Outline each uninfected red blood cell.
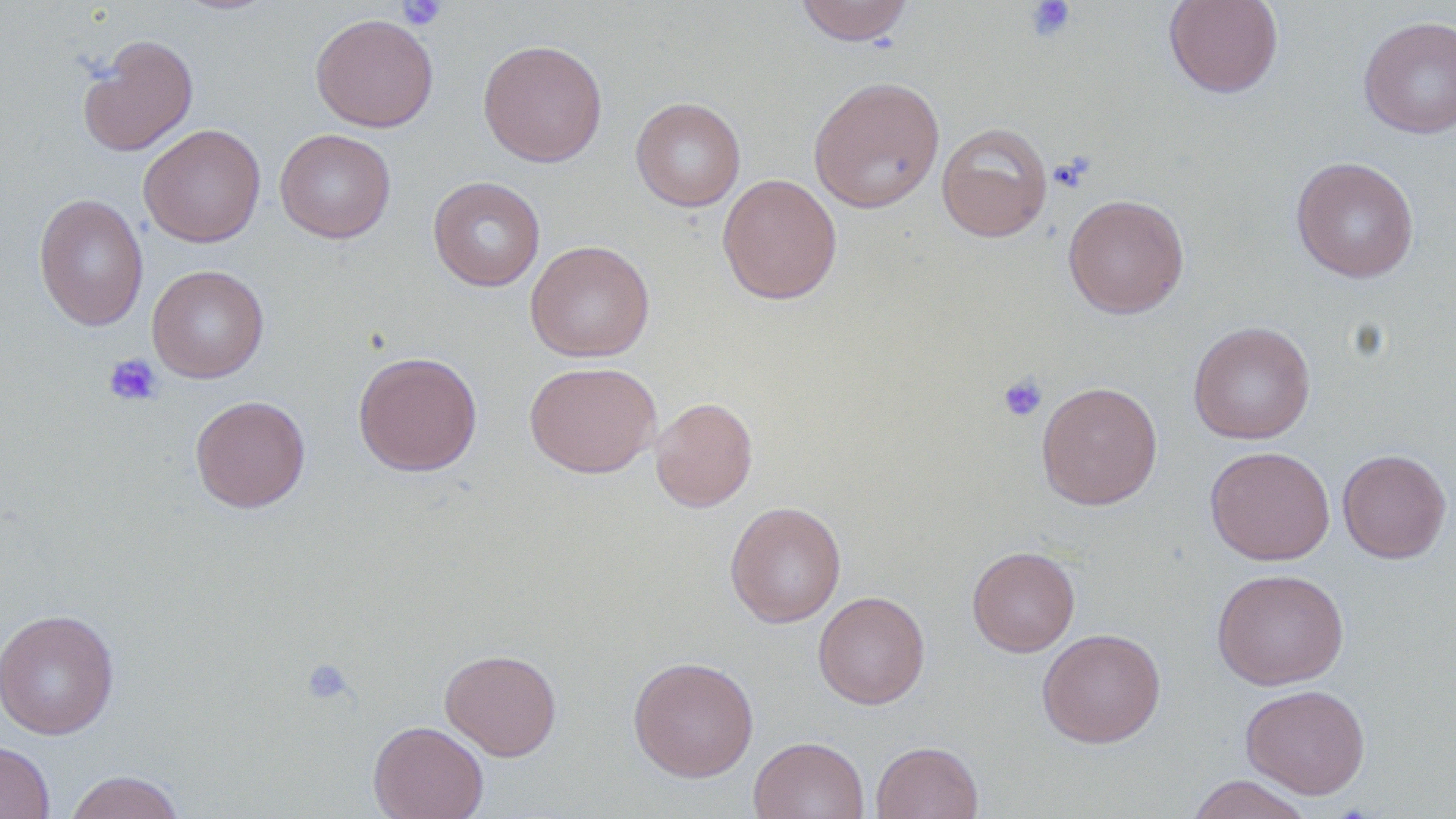
Approximate bounding boxes as (x1, y1, x2, y2) in pixels.
Uninfected red blood cells: (794, 0, 914, 46), (1163, 0, 1284, 98), (310, 13, 439, 132), (1358, 15, 1456, 138), (78, 34, 199, 156), (478, 39, 607, 167), (808, 75, 945, 214), (631, 97, 746, 212), (936, 122, 1053, 242), (138, 123, 266, 247), (275, 128, 396, 244), (1290, 156, 1419, 282), (717, 173, 842, 305), (428, 176, 545, 291), (33, 193, 149, 332), (1062, 193, 1189, 319), (525, 240, 654, 362), (147, 264, 269, 383), (1187, 321, 1316, 444), (353, 351, 483, 476), (523, 360, 661, 478), (1036, 381, 1163, 510), (190, 395, 311, 513), (650, 396, 758, 513), (1205, 446, 1335, 565), (1337, 448, 1452, 563), (725, 501, 847, 628), (967, 545, 1080, 657), (1211, 568, 1349, 690), (813, 591, 929, 709), (0, 608, 120, 740), (1037, 628, 1165, 748), (440, 647, 562, 761), (628, 656, 759, 782), (1241, 684, 1370, 799), (368, 720, 488, 819), (749, 736, 869, 819), (870, 740, 983, 818), (0, 741, 55, 819), (64, 770, 185, 819), (1185, 774, 1314, 819).

Platelet locations: (1024, 0, 1076, 42), (396, 1, 447, 31), (1049, 154, 1094, 193), (104, 353, 163, 407), (997, 373, 1048, 422), (301, 657, 355, 706). Slide-level diagnosis: negative for blood parasites. May-Grünwald-Giemsa-stained preparation. Image is 1456×819 pixels. Optical microscopy. Captured at 1000x magnification. Thin blood smear. Single field of view.